Give the location of every parasitized red blood cell.
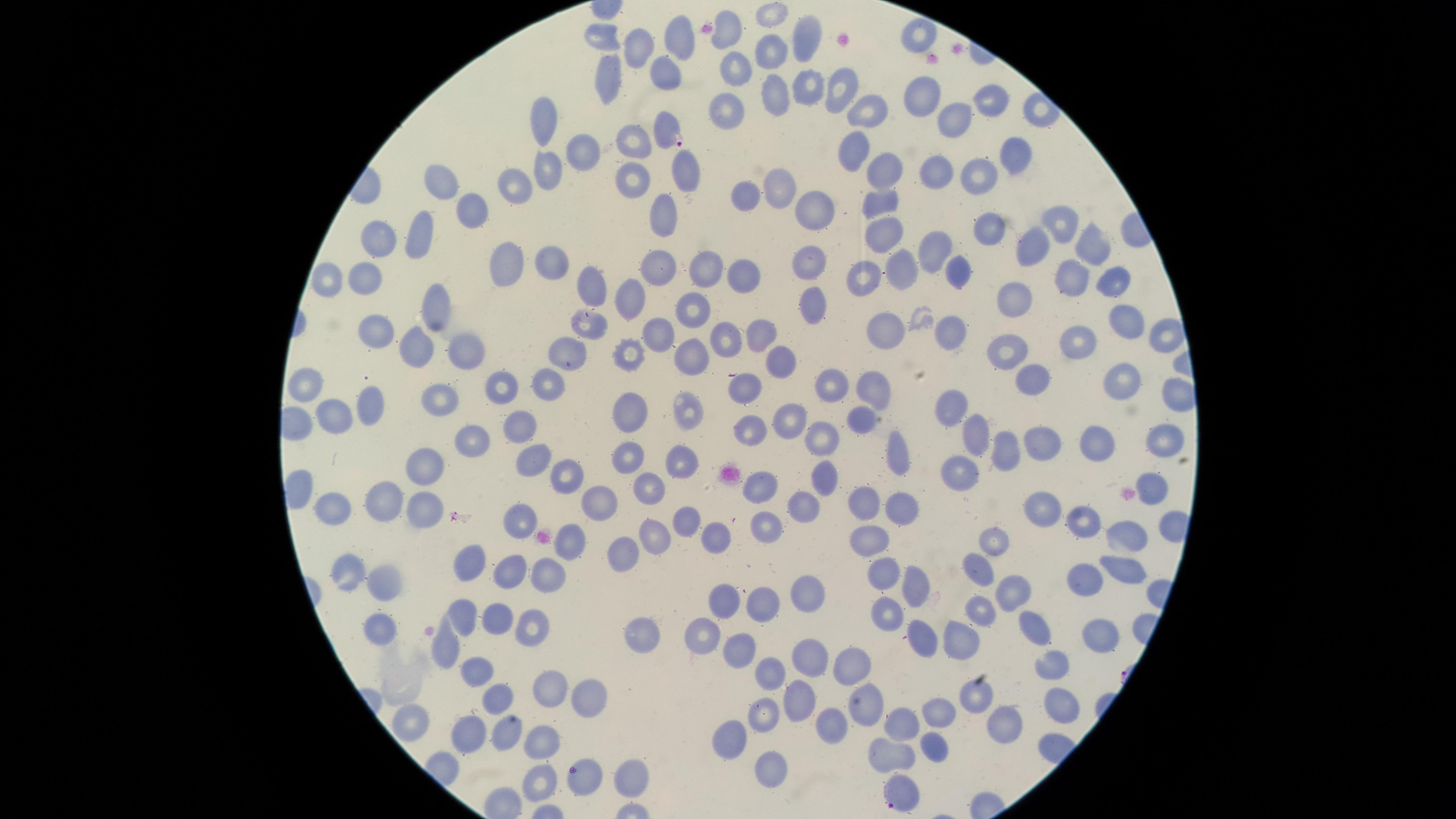
Approximate marker points, in pixels from the top-left corner.
Parasitized red blood cells: (x=669, y=130), (x=899, y=792).

Approximate marker points, in pixels from the top-left corner.
Summary:
  - Uninfected red blood cells: (x=773, y=15), (x=725, y=33), (x=919, y=34), (x=599, y=35), (x=806, y=39), (x=675, y=43), (x=634, y=47), (x=770, y=51), (x=733, y=69), (x=665, y=74), (x=612, y=77), (x=805, y=85), (x=840, y=87), (x=771, y=94), (x=923, y=96), (x=991, y=99), (x=725, y=112), (x=870, y=112), (x=545, y=119), (x=949, y=120), (x=636, y=137), (x=853, y=146), (x=585, y=152), (x=1009, y=155), (x=931, y=168), (x=681, y=169), (x=883, y=169), (x=548, y=170), (x=633, y=177), (x=978, y=179), (x=514, y=182), (x=443, y=183), (x=781, y=185), (x=746, y=192), (x=881, y=201), (x=476, y=207), (x=819, y=208), (x=665, y=216), (x=1058, y=219), (x=985, y=224), (x=883, y=236), (x=380, y=238), (x=417, y=243), (x=1036, y=243), (x=934, y=244), (x=1093, y=244), (x=507, y=261), (x=808, y=261), (x=548, y=262), (x=665, y=264), (x=699, y=266), (x=901, y=267), (x=961, y=272), (x=741, y=276), (x=366, y=278), (x=862, y=278), (x=1070, y=278), (x=1111, y=280), (x=326, y=281), (x=588, y=284), (x=1023, y=294), (x=635, y=299), (x=811, y=304), (x=435, y=311), (x=686, y=314), (x=1130, y=317), (x=590, y=320), (x=887, y=325), (x=762, y=326), (x=954, y=327), (x=380, y=333), (x=724, y=333), (x=662, y=336), (x=1163, y=338), (x=1077, y=343), (x=414, y=350), (x=630, y=350), (x=1014, y=350), (x=460, y=351), (x=573, y=354), (x=781, y=361), (x=691, y=362), (x=1033, y=376), (x=832, y=380), (x=1121, y=380), (x=551, y=383), (x=877, y=383), (x=745, y=386), (x=503, y=388), (x=308, y=391), (x=443, y=395), (x=373, y=400), (x=690, y=409), (x=952, y=410), (x=637, y=411), (x=863, y=414), (x=340, y=416), (x=792, y=417), (x=521, y=428), (x=752, y=430), (x=473, y=436), (x=974, y=437), (x=1166, y=437), (x=823, y=440), (x=1096, y=441), (x=1041, y=443), (x=1007, y=452), (x=899, y=453), (x=627, y=457), (x=529, y=460), (x=680, y=460), (x=428, y=463), (x=957, y=470), (x=559, y=474), (x=824, y=481), (x=761, y=483), (x=648, y=488), (x=390, y=499), (x=599, y=502), (x=908, y=502), (x=866, y=504), (x=809, y=505), (x=1047, y=505), (x=338, y=507), (x=424, y=509), (x=683, y=516), (x=1085, y=518), (x=518, y=519), (x=769, y=520), (x=723, y=535), (x=1123, y=535), (x=651, y=537), (x=1001, y=538), (x=872, y=542), (x=572, y=544), (x=620, y=551), (x=468, y=562), (x=509, y=564), (x=979, y=566), (x=348, y=571), (x=548, y=571), (x=1120, y=572), (x=1088, y=574), (x=889, y=579), (x=380, y=581), (x=914, y=583), (x=1009, y=593), (x=801, y=595), (x=762, y=602), (x=725, y=605), (x=981, y=606), (x=494, y=611), (x=888, y=614), (x=462, y=616), (x=536, y=621), (x=1040, y=628), (x=377, y=629), (x=705, y=630), (x=641, y=635), (x=919, y=638), (x=1101, y=641), (x=970, y=646), (x=742, y=648), (x=446, y=651), (x=807, y=655), (x=857, y=663), (x=1048, y=666), (x=480, y=669), (x=773, y=672), (x=554, y=686), (x=590, y=691), (x=976, y=699), (x=492, y=704), (x=799, y=704), (x=874, y=704), (x=1056, y=704), (x=767, y=712), (x=938, y=717), (x=410, y=721), (x=999, y=722), (x=904, y=723), (x=829, y=724), (x=468, y=733), (x=506, y=735), (x=538, y=739), (x=729, y=743), (x=931, y=748), (x=892, y=750), (x=771, y=762), (x=630, y=775), (x=584, y=777), (x=542, y=781)
  - Visible region: circular
  - Image size: 1456×819 pixels
  - Capture: smartphone photograph through the microscope eyepiece
  - Species: Plasmodium falciparum
  - Field of view: single
  - Stain: Giemsa
  - Preparation: thin blood film